Assess this cell for malaria.
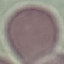

Uninfected.

preparation = thin blood film
capture = smartphone camera at the microscope eyepiece
image type = cell patch, automatically extracted from a larger field of view and resized to 64 × 64 pixels
stain = Giemsa